Assess the morphology of the red blood cells.
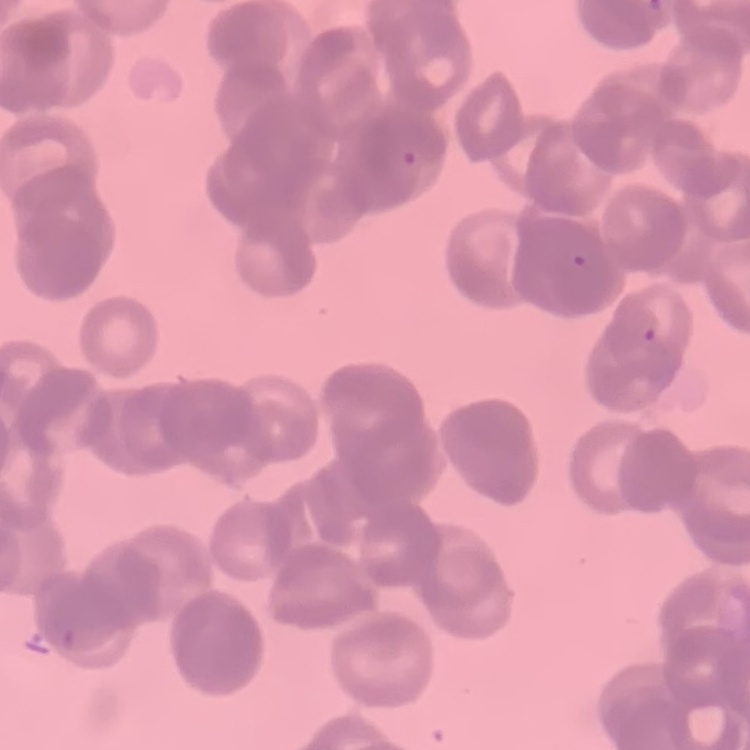
They show rouleaux formation.

Summary:
  - Stain: Field's or Giemsa
  - Image type: square crop of a larger photomicrograph
  - Preparation: thin peripheral smear